Report the malaria status.
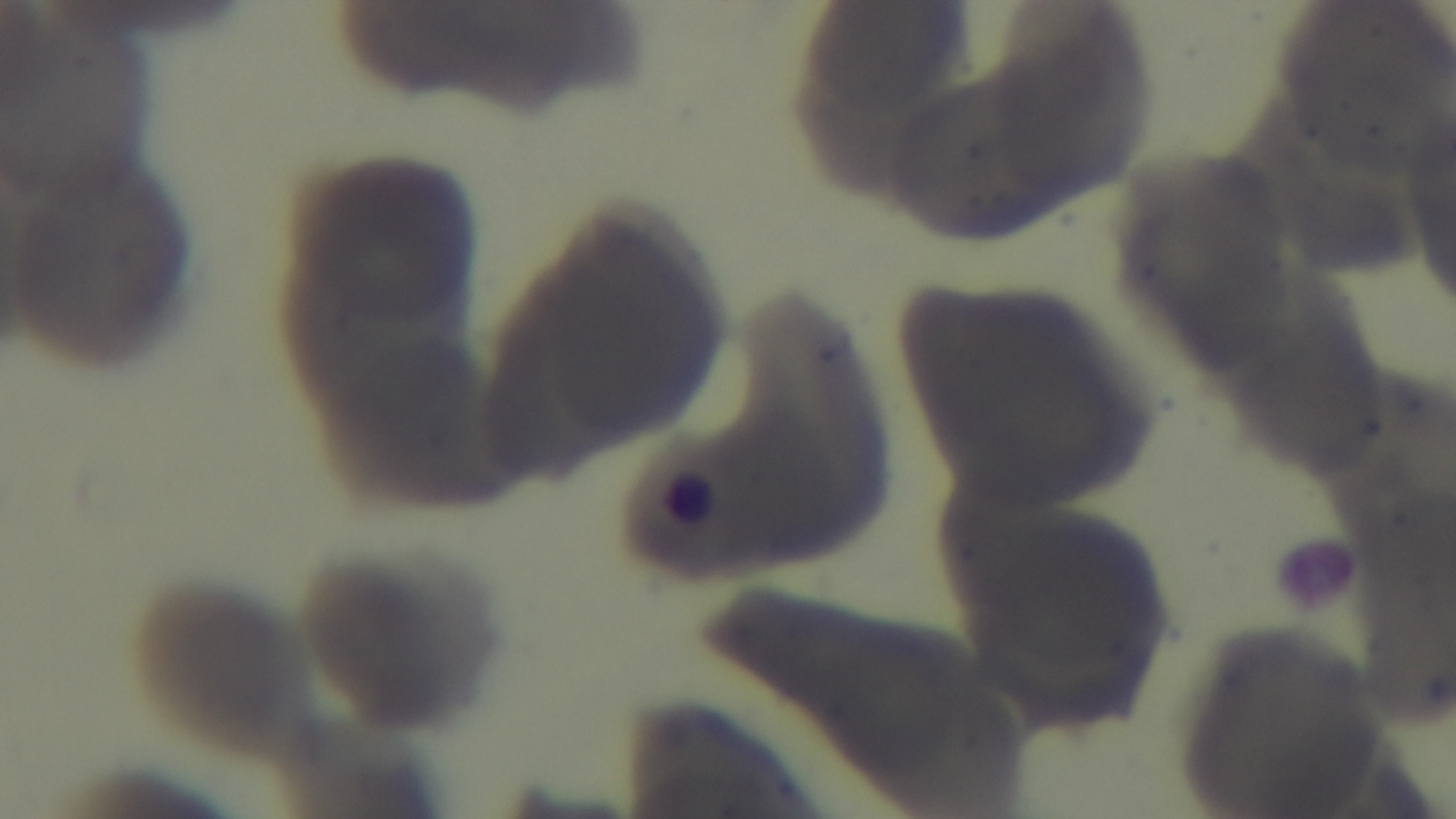

Uninfected.

Summary:
  - Modality: light microscopy
  - Capture: mounted 4K digital camera
  - Stain: Giemsa
  - Field of view: one from the slide
  - Objective: 100x oil immersion
  - Preparation: thin